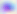

identification: Toxoplasma gondii
magnification: 400x
modality: micrograph